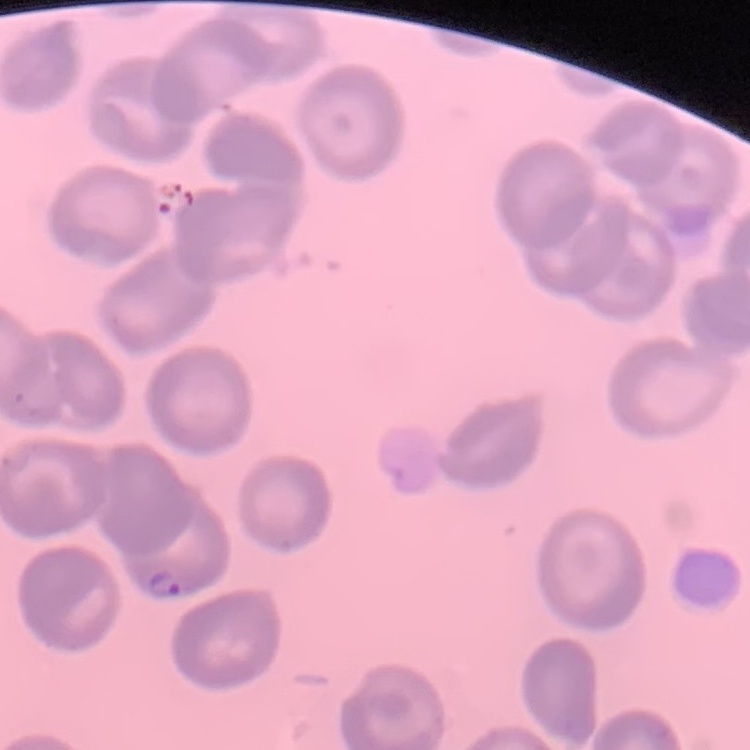 The erythrocytes exhibit no rouleaux formation. Thin blood film. Square crop of a larger photomicrograph. Stained with either Field's or Giemsa.